State which parasite is depicted.
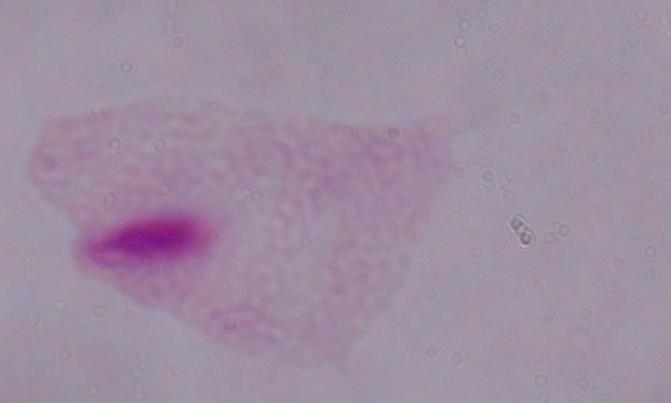

A trichomonad.

Captured at 1000x magnification. Micrograph.